Assess this cell for malaria.
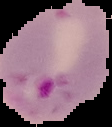

Parasitized.

Segmented cell region on a black background. From a thin blood smear. Image is 112×127 pixels.